Classify this cell by malaria status.
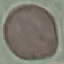
Uninfected.

image type = cell patch, automatically extracted from a larger field of view and resized to 64 × 64 pixels
preparation = thin blood film
capture = smartphone camera at the microscope eyepiece
stain = Giemsa